Assess this cell for malaria.
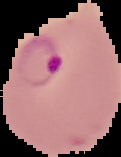
Parasitized.

image_size: 121×157 pixels
preparation: thin blood smear
image_type: cell region segmented out of the field of view; surrounding area masked to black